Describe the morphology of the red blood cells.
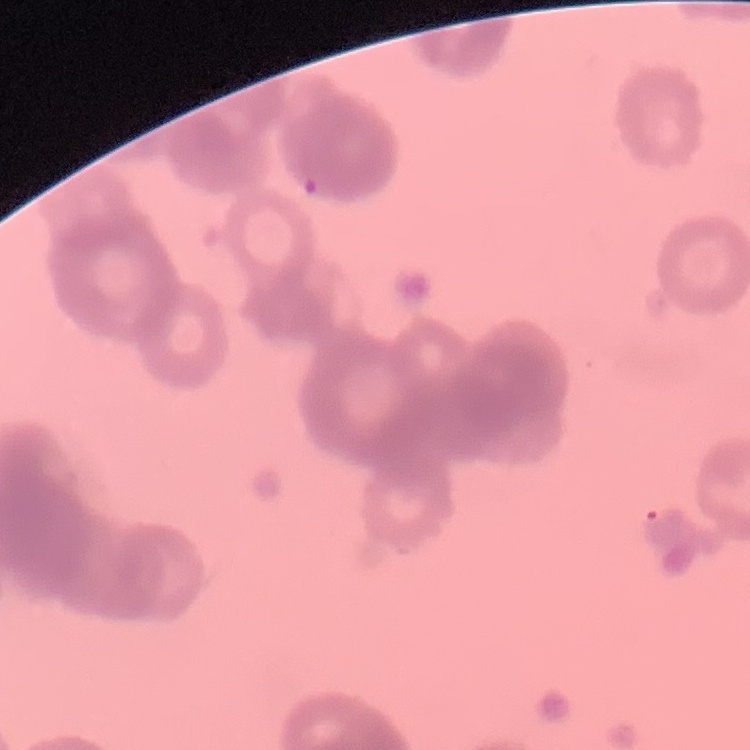
They show rouleaux formation.

One tile cut from a larger photomicrograph. Field's or Giemsa stain. Thin blood smear.